Identify the cell.
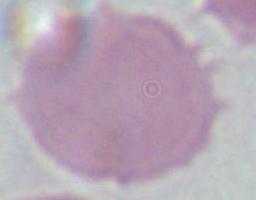
This is an erythrocyte.

1000x magnification. Micrograph.